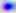

Micrograph. Captured at 400x magnification. Toxoplasma gondii is shown.